Assess for Plasmodium parasites.
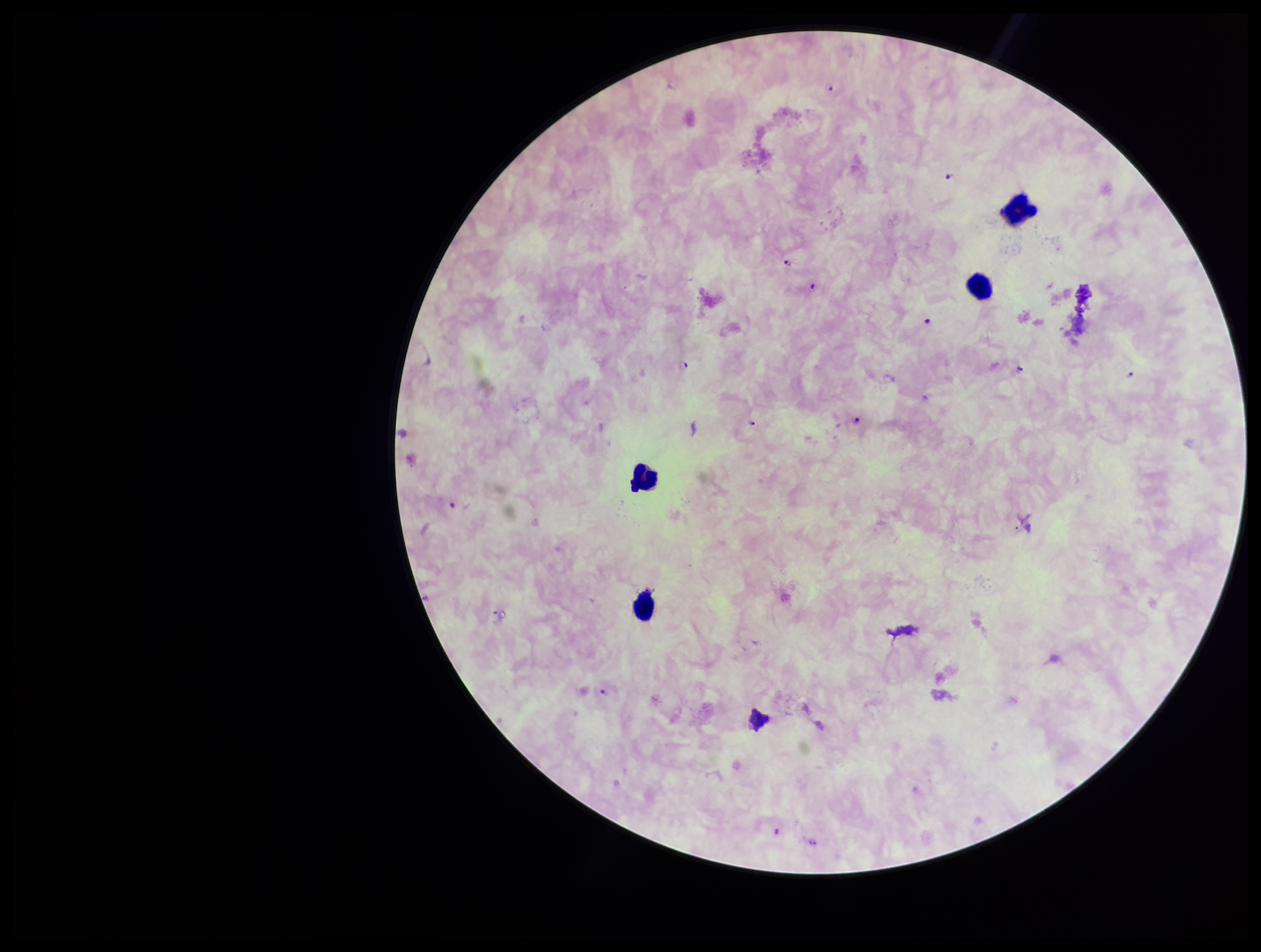
Detected.

Patient malaria status: infected. Stained with Giemsa. One field from this slide. Smartphone photograph taken through the eyepiece of a microscope. Parasite count: 12. Preparation: thick blood smear. Leukocyte count: 4. Image is 1261×952 pixels. Species reported for this patient: Plasmodium falciparum.